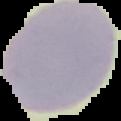

Summary:
  - Image size: 121×121 pixels
  - Image type: segmented cell region on a black background
  - Malaria status: uninfected
  - Preparation: thin blood film